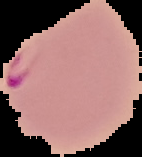

Result: malaria parasites detected. From a thin blood film. Image is 142×157 pixels. The area outside the segmented cell region is set to black.